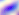
Summary:
  - Modality: micrograph
  - Identification: Toxoplasma gondii
  - Magnification: 400x